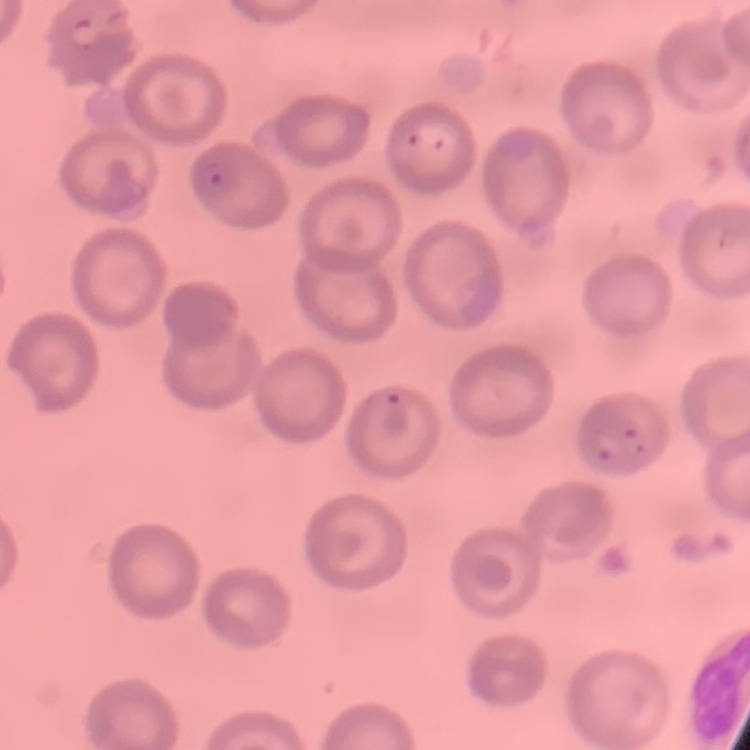
Summary:
  - Erythrocyte morphology: no rouleaux formation
  - Stain: Field's or Giemsa
  - Preparation: thin blood film
  - Image type: square crop of a larger photomicrograph